Assess the morphology of the red blood cells.
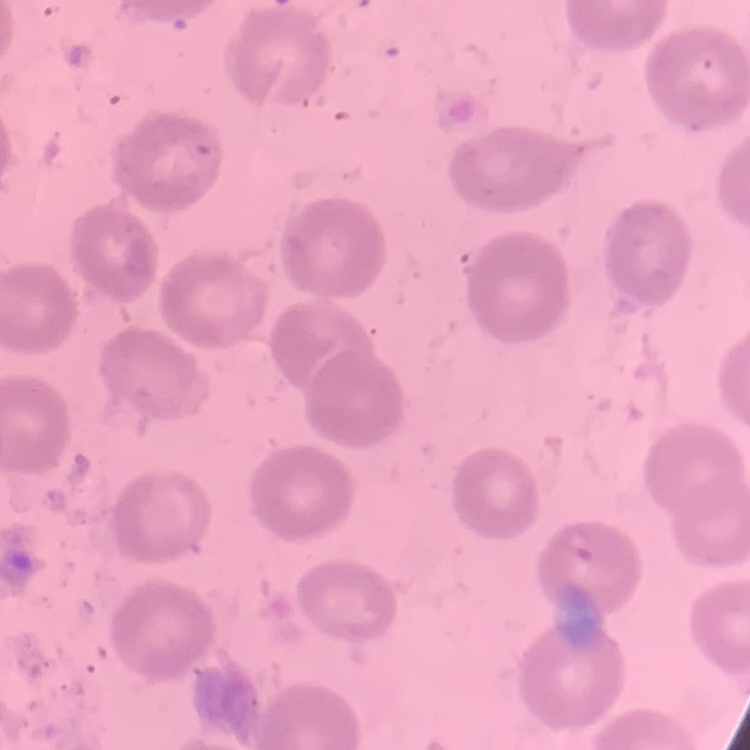
They show no rouleaux formation.

Thin blood film. One tile cut from a larger photomicrograph. Field's or Giemsa stain.